Assess this cell for malaria.
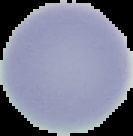

It is uninfected.

Summary:
  - Image size: 133×136 pixels
  - Image type: cell region segmented out of the field of view; surrounding area masked to black
  - Preparation: thin blood smear